Point out each malaria parasite.
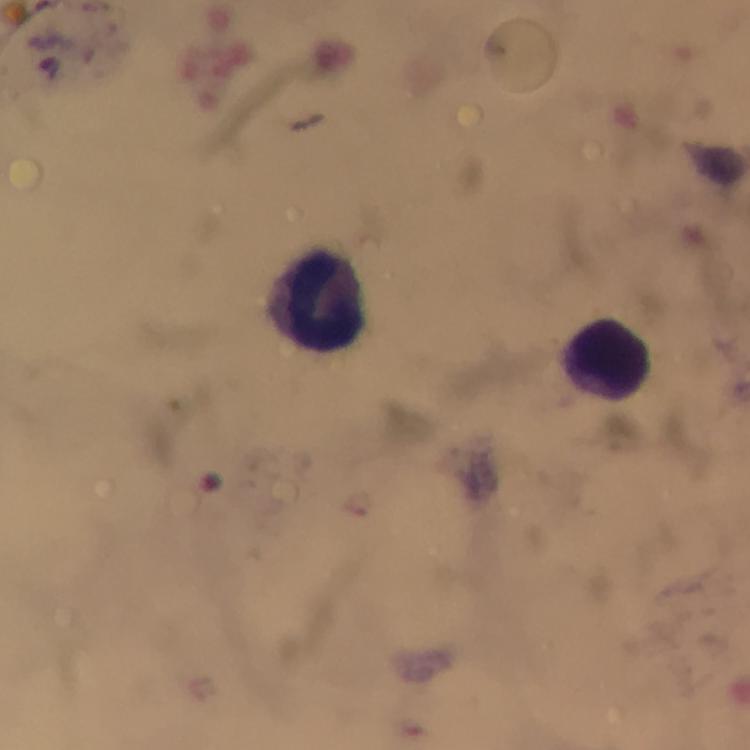
No malaria parasites seen.

Approximate centers as (x, y) in pixels.
Summary:
  - Leukocyte locations: (317, 301), (601, 360)
  - Capture: smartphone camera through the microscope
  - Stain: Giemsa
  - Magnification: 100x
  - Immersion oil: applied
  - Context: from a malaria diagnostic workup
  - Preparation: thick smear
  - Image size: 750×750 pixels
  - Cropped from: one field of view